State the blood parasite species.
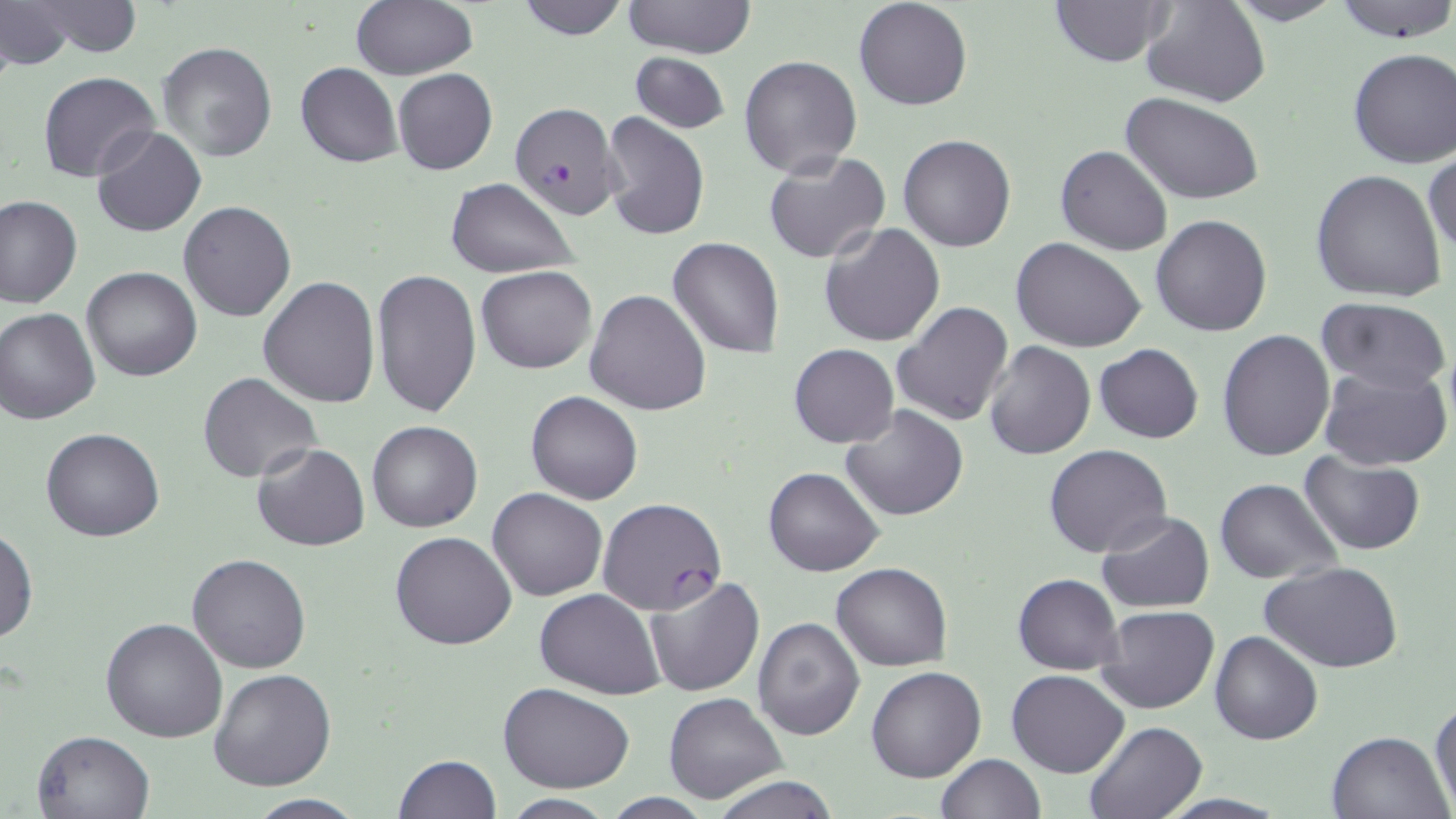

Plasmodium falciparum.

preparation = thin blood smear
image size = 1456×819 pixels
Plasmodium falciparum-infected red blood cell locations = approximate bounding boxes as [x1, y1, x2, y2] in pixels: [508, 101, 623, 220], [597, 496, 727, 615]
modality = light microscopy
field of view = single
uninfected red blood cell locations = approximate bounding boxes as [x1, y1, x2, y2] in pixels: [0, 0, 77, 70], [350, 0, 476, 80], [515, 0, 630, 39], [853, 0, 973, 111], [1049, 0, 1174, 67], [1142, 0, 1271, 107], [1226, 0, 1346, 27], [1333, 0, 1456, 43], [27, 1, 144, 58], [621, 1, 755, 57], [322, 8, 468, 128], [157, 41, 278, 162], [1347, 48, 1456, 169], [628, 52, 731, 133], [739, 54, 861, 178], [295, 63, 403, 167], [393, 68, 497, 176], [38, 71, 162, 183], [1120, 92, 1264, 205], [600, 111, 709, 243], [92, 124, 206, 238], [898, 134, 1016, 253], [1055, 145, 1173, 255], [1424, 150, 1455, 264], [764, 151, 891, 263], [1310, 168, 1447, 303], [445, 176, 580, 278], [0, 196, 81, 309], [178, 202, 296, 322], [1151, 214, 1272, 336], [819, 223, 945, 348], [668, 236, 786, 359], [1012, 238, 1148, 353], [477, 265, 597, 374], [81, 266, 200, 381], [371, 268, 481, 416], [259, 277, 380, 408], [585, 288, 712, 414], [1316, 298, 1455, 396], [891, 302, 1014, 427], [0, 308, 100, 424], [1218, 328, 1335, 463], [983, 339, 1096, 459], [1094, 343, 1203, 443], [789, 344, 897, 447], [1321, 363, 1454, 471], [198, 373, 322, 483], [526, 389, 643, 504], [839, 406, 968, 520], [367, 421, 482, 532], [42, 428, 164, 543], [251, 442, 370, 553], [1043, 443, 1172, 558], [1300, 451, 1423, 556], [763, 466, 883, 577], [1214, 479, 1344, 583], [487, 488, 608, 601], [1097, 510, 1216, 612], [0, 526, 37, 644], [389, 532, 516, 651], [186, 554, 312, 673], [832, 561, 953, 671], [1262, 561, 1403, 673], [1013, 572, 1124, 674], [642, 574, 764, 697], [535, 588, 665, 700], [1095, 604, 1219, 714], [101, 616, 228, 743], [752, 616, 865, 739], [1210, 631, 1323, 745], [865, 666, 986, 782], [209, 669, 337, 791], [1007, 670, 1129, 777], [498, 682, 635, 792], [662, 692, 788, 805], [1430, 698, 1456, 812], [1082, 720, 1207, 819], [31, 728, 154, 818], [1327, 730, 1453, 818], [935, 752, 1046, 819], [394, 754, 503, 818], [711, 775, 838, 819], [242, 795, 369, 818], [499, 795, 620, 818]
stain = May-Grünwald-Giemsa
magnification = 1000x